Assess this cell for malaria.
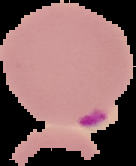

It is parasitized.

preparation = thin blood film
image size = 136×166 pixels
image type = cell region segmented out of the field of view; surrounding area masked to black